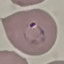
Result: malaria parasites detected. Automatically extracted cell patch, resized to 64 × 64 pixels. Acquired by smartphone through the microscope eyepiece. Thin smear of blood. Giemsa-stained preparation.